Locate and identify every blood parasite.
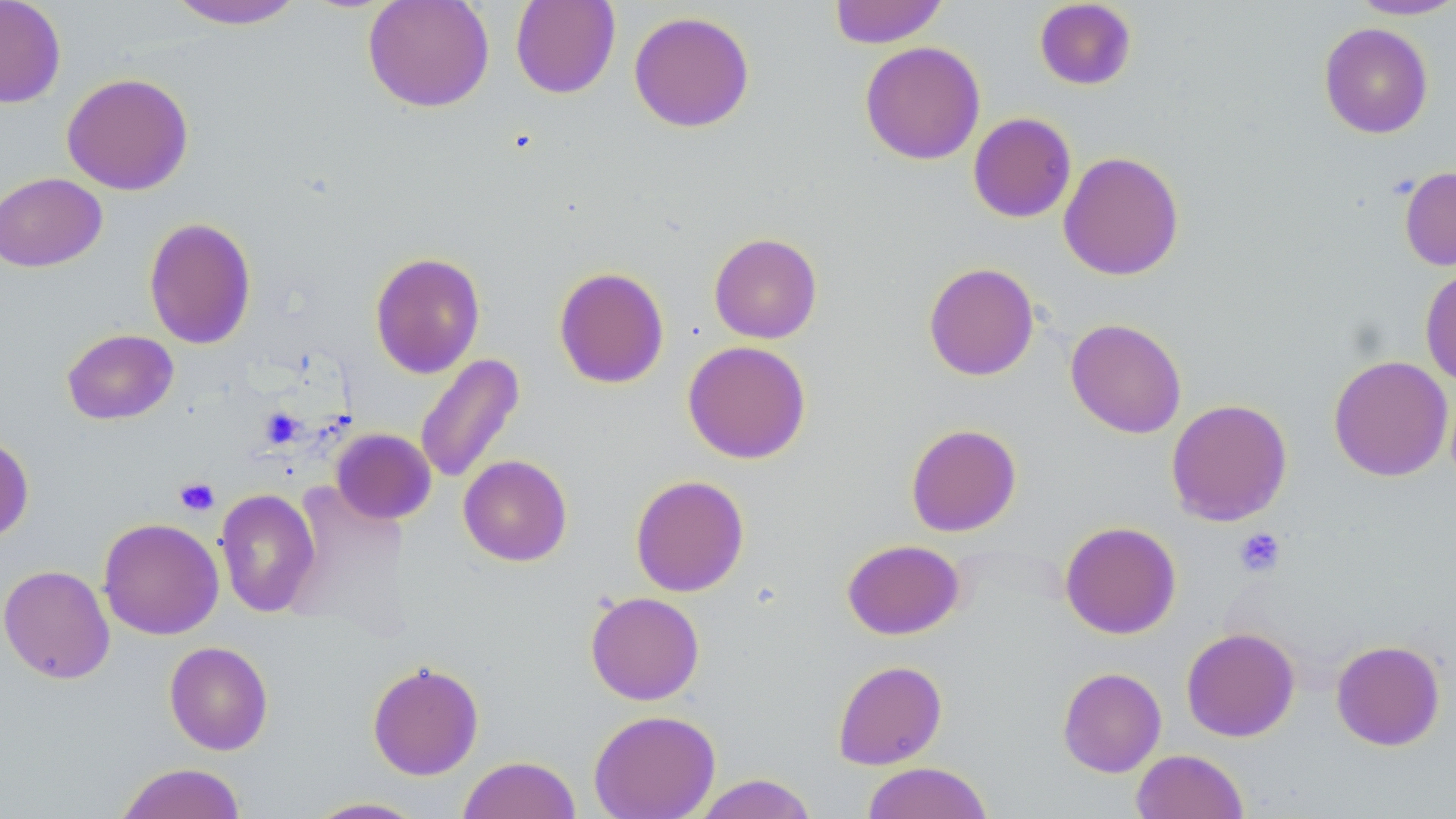
No blood parasites observed.

Approximate bounding boxes as (x1,y1)-(x2,y2) corner pairs in pixels. Uninfected red blood cell locations: (0,0)-(66,108), (164,0)-(308,30), (362,0)-(494,113), (510,0)-(620,99), (829,0)-(948,48), (1348,0)-(1456,20), (1034,1)-(1137,90), (628,10)-(755,133), (1319,22)-(1434,138), (860,41)-(985,165), (61,72)-(194,195), (968,112)-(1076,223), (1058,151)-(1184,281), (1399,166)-(1456,270), (0,172)-(107,272), (143,216)-(256,350), (709,232)-(822,344), (369,251)-(486,378), (923,262)-(1039,381), (553,266)-(670,389), (1420,266)-(1456,385), (1065,318)-(1187,438), (62,329)-(179,425), (682,340)-(811,464), (415,353)-(524,485), (1328,355)-(1453,481), (1166,398)-(1293,526), (905,423)-(1022,537), (331,428)-(436,525), (0,431)-(34,544), (458,455)-(573,566), (630,474)-(749,597), (215,488)-(321,618), (98,517)-(224,640), (1060,520)-(1181,639), (841,539)-(965,640), (0,564)-(116,684), (585,591)-(705,705), (1181,627)-(1300,742), (1330,639)-(1446,751), (164,641)-(273,755), (832,660)-(947,769), (367,661)-(484,780), (1057,667)-(1167,778), (588,709)-(720,819), (1131,749)-(1249,819), (458,755)-(582,819), (114,762)-(248,819), (861,762)-(993,819), (692,773)-(819,819), (305,797)-(430,818). Platelet locations: (259,408)-(305,449), (174,477)-(220,516), (1234,527)-(1286,578). Slide-level diagnosis: no evidence of blood parasites. One field of a larger specimen. Thin blood film. Image is 1456×819 pixels. May-Grünwald-Giemsa-stained preparation. Light microscopy. Captured at 1000x magnification.